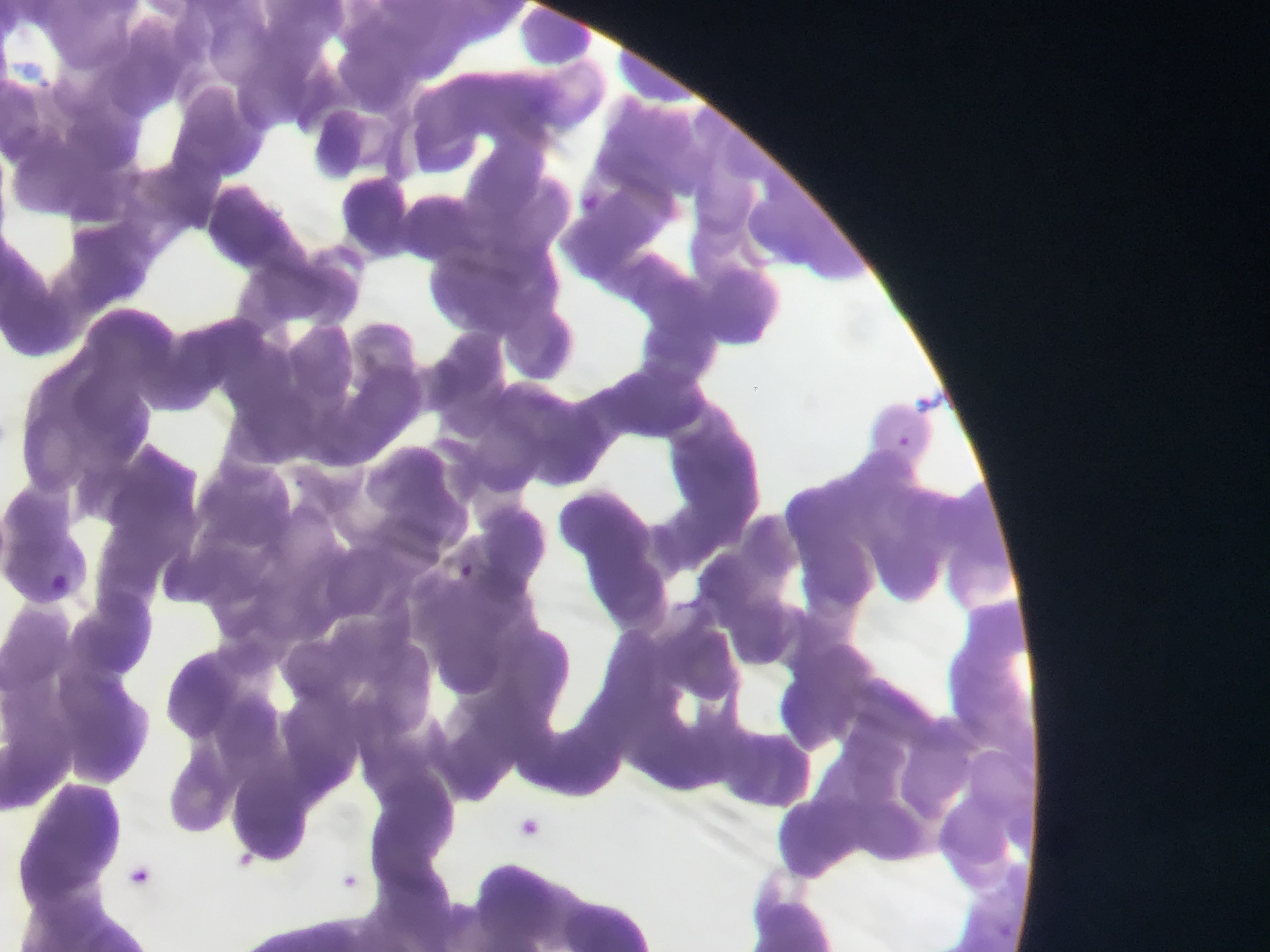
Approximate bounding boxes as [left, top, right, bottom] in pixels. Plasmodium parasite locations: [582, 187, 608, 216], [913, 388, 944, 414], [898, 435, 927, 457], [460, 563, 475, 577], [51, 570, 78, 587], [520, 814, 550, 839], [236, 839, 268, 872], [125, 862, 163, 889], [342, 865, 368, 895]. Image is 1270×952 pixels. Thin blood smear. Sample from Ghana. One field of view. Photographed through a microscope with a mobile-phone camera.